Outline platelets.
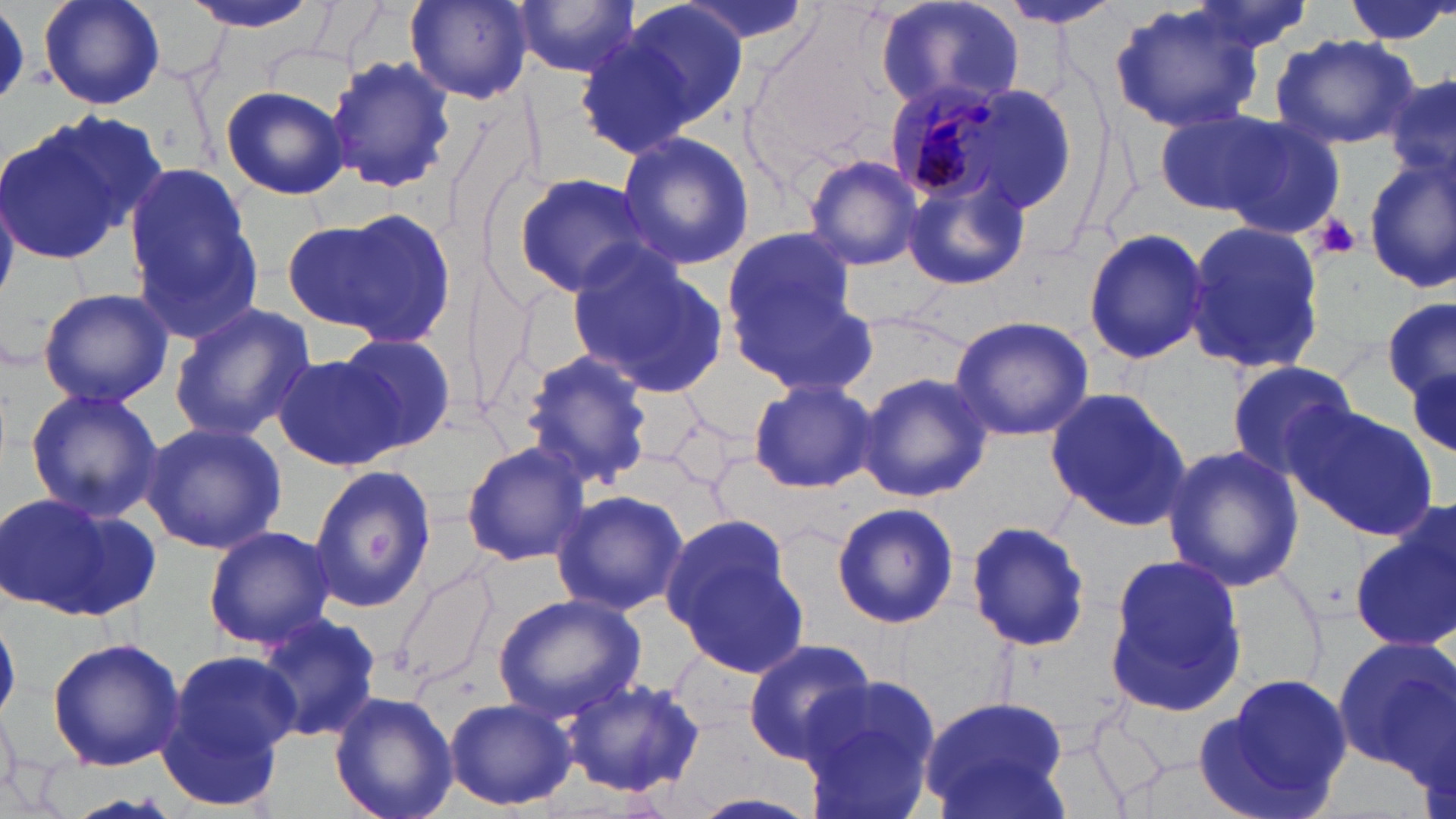

Approximate bounding boxes as [x1, y1, x2, y2] in pixels.
Platelets: [1312, 213, 1361, 260].

Summary:
  - Uninfected red blood cell locations: [39, 0, 164, 109], [179, 0, 328, 36], [405, 0, 532, 105], [512, 0, 638, 79], [671, 0, 818, 53], [1340, 0, 1453, 47], [1177, 1, 1319, 58], [612, 2, 748, 133], [874, 2, 1026, 117], [996, 2, 1128, 31], [1108, 3, 1266, 135], [0, 7, 32, 103], [575, 27, 693, 159], [1271, 33, 1420, 151], [325, 54, 456, 195], [1386, 68, 1456, 195], [217, 85, 350, 199], [1154, 106, 1291, 218], [1218, 115, 1348, 242], [0, 121, 135, 266], [615, 130, 755, 271], [802, 153, 924, 271], [1361, 155, 1456, 296], [120, 163, 261, 341], [901, 168, 1030, 292], [513, 174, 658, 298], [289, 204, 460, 346], [1184, 218, 1324, 379], [1083, 226, 1211, 365], [717, 229, 871, 384], [568, 252, 729, 396], [466, 265, 539, 425], [36, 285, 175, 408], [1383, 298, 1456, 405], [169, 302, 317, 441], [948, 314, 1096, 440], [333, 331, 457, 453], [516, 350, 655, 492], [274, 354, 397, 469], [1404, 360, 1456, 471], [1224, 361, 1360, 481], [856, 372, 994, 503], [748, 379, 878, 493], [1045, 386, 1193, 532], [25, 387, 163, 522], [1287, 404, 1438, 539], [141, 420, 287, 555], [460, 441, 590, 566], [1161, 443, 1306, 594], [307, 465, 437, 614], [549, 487, 689, 618], [0, 493, 158, 622], [831, 501, 959, 629], [1355, 513, 1456, 651], [662, 514, 810, 677], [964, 518, 1092, 652], [203, 526, 336, 649], [1102, 554, 1246, 717], [392, 562, 502, 696], [494, 593, 645, 721], [252, 610, 382, 746], [47, 636, 188, 770], [1331, 637, 1454, 776], [740, 639, 876, 764], [157, 649, 299, 804], [1196, 674, 1355, 816], [561, 675, 709, 798], [801, 677, 943, 818], [328, 689, 457, 819], [916, 696, 1072, 819], [444, 697, 577, 811], [688, 793, 825, 819]
  - Plasmodium malariae-infected red blood cell locations: [889, 78, 1007, 203]
  - Slide-level diagnosis: Plasmodium malariae
  - Magnification: 1000x
  - Field of view: one of a larger specimen
  - Image size: 1456×819 pixels
  - Stain: May-Grünwald-Giemsa
  - Preparation: thin blood film
  - Modality: optical microscopy